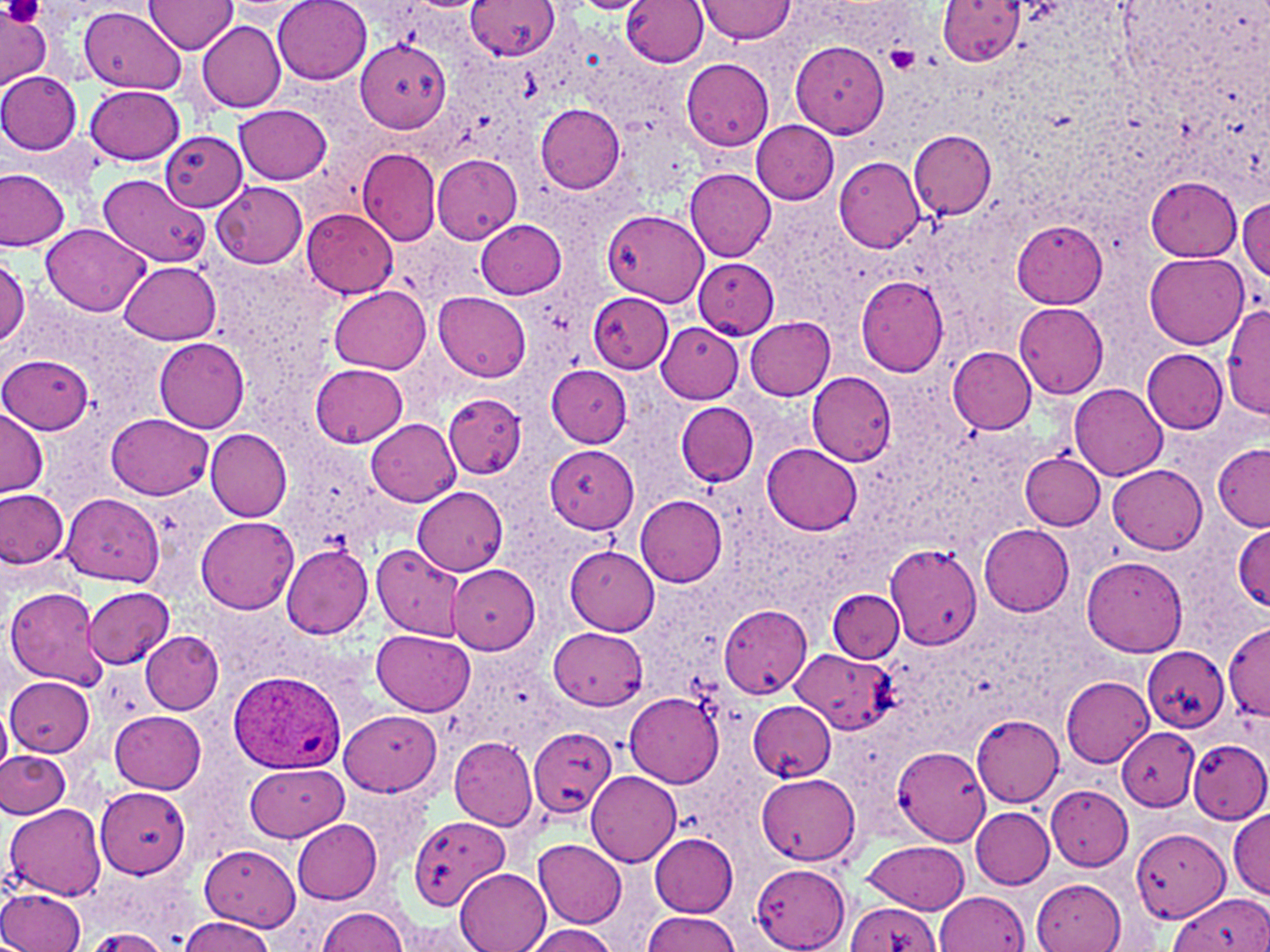
Summary:
  - Coordinate format: approximate bounding boxes as (x1, y1, x2, y2) in pixels
  - Uninfected red blood cell locations: (274, 0, 371, 84), (468, 0, 561, 62), (697, 0, 795, 43), (149, 1, 238, 53), (566, 1, 654, 15), (620, 1, 707, 69), (938, 1, 1026, 68), (223, 3, 313, 21), (80, 6, 186, 95), (0, 8, 55, 90), (197, 21, 286, 112), (354, 37, 451, 133), (790, 40, 890, 138), (680, 57, 775, 151), (0, 72, 82, 153), (86, 83, 185, 163), (536, 103, 625, 193), (234, 104, 331, 182), (752, 122, 839, 204), (161, 129, 247, 211), (908, 130, 996, 217), (360, 148, 441, 245), (433, 153, 523, 243), (834, 154, 924, 253), (0, 168, 69, 252), (685, 168, 775, 261), (96, 175, 212, 268), (1146, 176, 1242, 261), (212, 180, 308, 268), (1237, 197, 1269, 283), (303, 208, 398, 298), (603, 209, 708, 307), (475, 219, 565, 297), (1012, 219, 1107, 308), (42, 224, 150, 316), (1144, 250, 1248, 349), (0, 256, 29, 349), (693, 256, 779, 339), (119, 261, 221, 344), (855, 275, 948, 377), (329, 285, 430, 373), (434, 292, 531, 383), (589, 292, 673, 372), (1014, 303, 1108, 398), (1223, 304, 1270, 415), (744, 316, 836, 399), (657, 323, 744, 403), (154, 337, 249, 433), (948, 347, 1037, 433), (1144, 349, 1228, 433), (0, 355, 92, 433), (310, 363, 408, 447), (547, 366, 632, 446), (807, 371, 896, 465), (1070, 384, 1167, 482), (442, 393, 526, 478), (677, 402, 758, 485), (0, 407, 48, 497), (106, 414, 213, 500), (367, 419, 461, 507), (205, 427, 292, 521), (1212, 441, 1270, 530), (763, 443, 863, 534), (545, 444, 638, 533), (1020, 450, 1104, 529), (1108, 465, 1207, 553), (413, 486, 509, 575), (1, 489, 70, 569), (62, 495, 163, 585), (635, 495, 726, 587), (198, 516, 299, 613), (1233, 521, 1270, 614), (979, 524, 1073, 615), (884, 543, 982, 651), (372, 544, 465, 640), (281, 545, 372, 639), (566, 547, 660, 636), (1082, 557, 1188, 657), (449, 567, 541, 654), (83, 586, 175, 669), (5, 587, 105, 689), (829, 588, 905, 663), (719, 603, 811, 699), (1224, 624, 1268, 722), (548, 625, 647, 707), (372, 629, 475, 715), (139, 631, 222, 713), (1140, 645, 1231, 732), (792, 648, 895, 735), (1062, 675, 1153, 766), (6, 676, 96, 756), (625, 692, 723, 785), (747, 700, 836, 781), (0, 703, 11, 777), (341, 708, 443, 796), (110, 710, 206, 795), (972, 714, 1063, 806), (1118, 726, 1198, 811), (528, 727, 618, 819), (450, 738, 538, 829), (1187, 738, 1270, 823), (893, 747, 991, 844), (0, 750, 70, 818), (245, 762, 349, 841), (585, 770, 681, 867), (754, 775, 858, 864), (95, 785, 191, 879), (1046, 785, 1134, 871), (6, 804, 106, 899), (969, 807, 1055, 889), (1228, 810, 1270, 896), (408, 818, 516, 921), (292, 821, 381, 902), (1131, 827, 1230, 925), (651, 834, 738, 916), (534, 839, 627, 926), (861, 841, 970, 914), (199, 845, 302, 928), (752, 862, 849, 952), (456, 868, 551, 952), (1032, 876, 1127, 951), (0, 887, 85, 951), (933, 892, 1028, 952), (1172, 892, 1270, 952), (844, 902, 944, 952), (316, 907, 411, 951), (642, 911, 739, 951), (180, 917, 276, 951), (387, 920, 489, 951), (518, 924, 620, 952), (82, 928, 176, 951)
  - Platelet locations: (3, 0, 44, 25), (883, 46, 920, 76)
  - Plasmodium ovale-infected red blood cell locations: (231, 670, 352, 780)
  - Slide-level diagnosis: Plasmodium ovale
  - Stain: May-Grünwald-Giemsa
  - Field of view: single
  - Modality: light microscopy
  - Image size: 1270×952 pixels
  - Preparation: thin blood film
  - Magnification: 1000x